Assess the morphology of the erythrocytes.
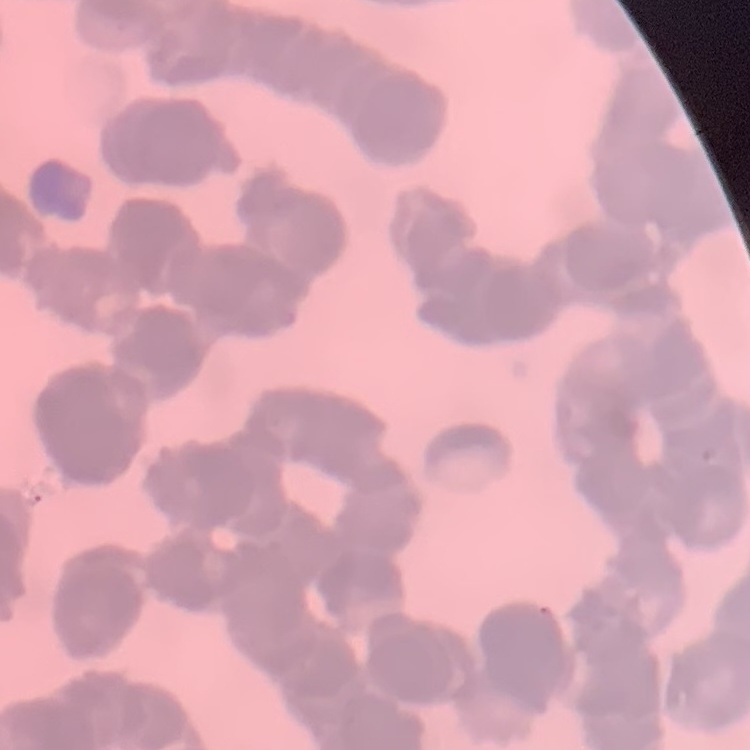
Rouleaux formation.

image type = one tile cut from a larger photomicrograph
preparation = thin blood film
stain = Field's or Giemsa